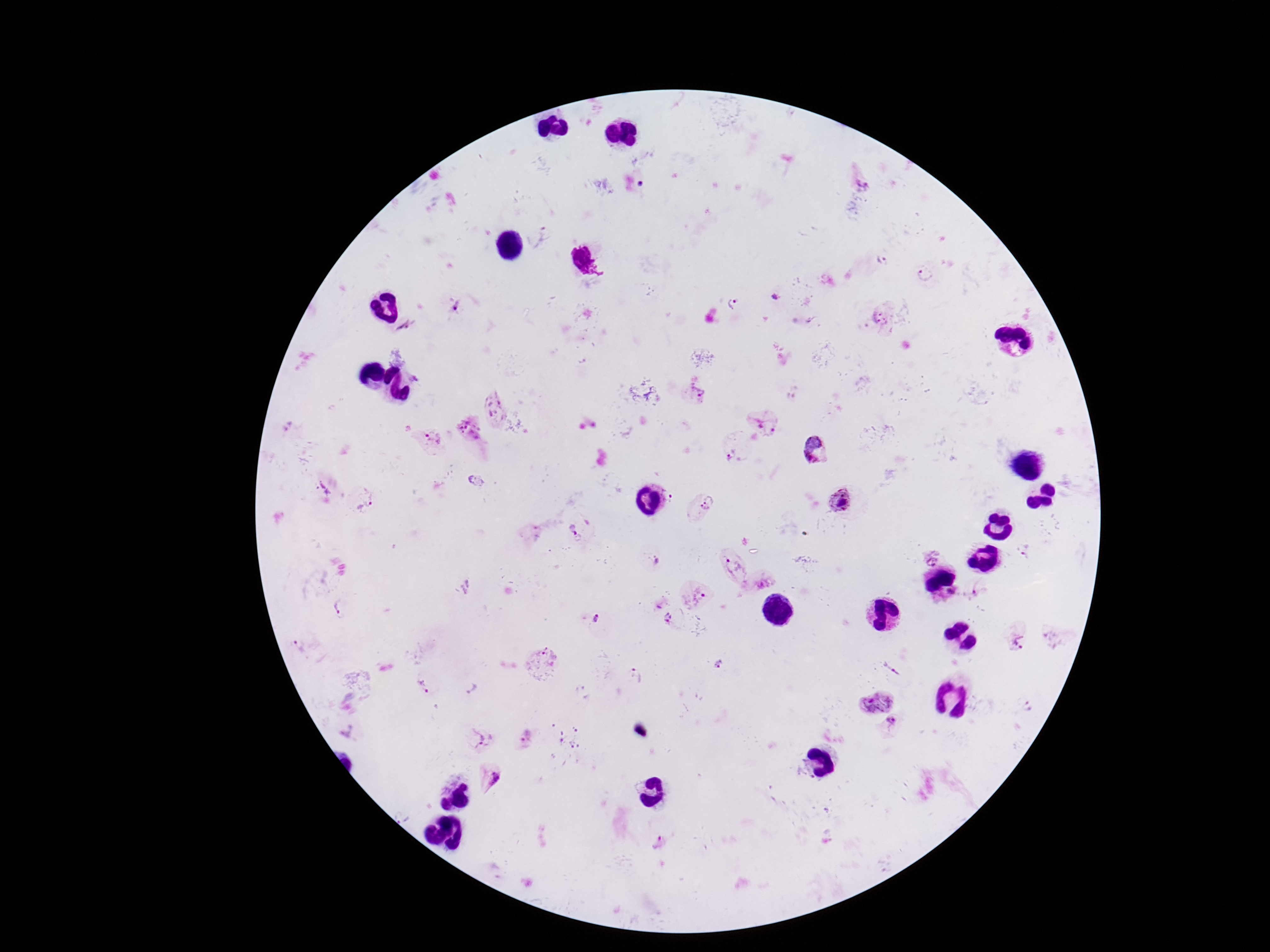
Approximate centers as (x, y) in pixels.
Summary:
  - Plasmodium parasite locations: (860, 173), (539, 238), (881, 262), (925, 274), (775, 299), (737, 304), (453, 307), (880, 316), (406, 326), (695, 394), (492, 408), (764, 420), (469, 432), (433, 439), (737, 449), (815, 450), (362, 499), (842, 502), (701, 510), (580, 526), (1024, 552), (930, 556), (733, 564), (764, 583), (981, 585), (948, 592), (696, 595), (341, 607), (669, 617), (595, 618), (1016, 637), (299, 646), (543, 658), (719, 664), (894, 667), (635, 674), (425, 686), (471, 687), (873, 697), (1028, 706), (893, 722), (482, 736), (523, 738), (488, 778), (658, 841)
  - Stain: Giemsa
  - Image size: 1270×952 pixels
  - Capture: smartphone camera through the microscope eyepiece
  - Field of view: single
  - Magnification: 100x
  - Patient malaria status: positive
  - Preparation: thick blood film